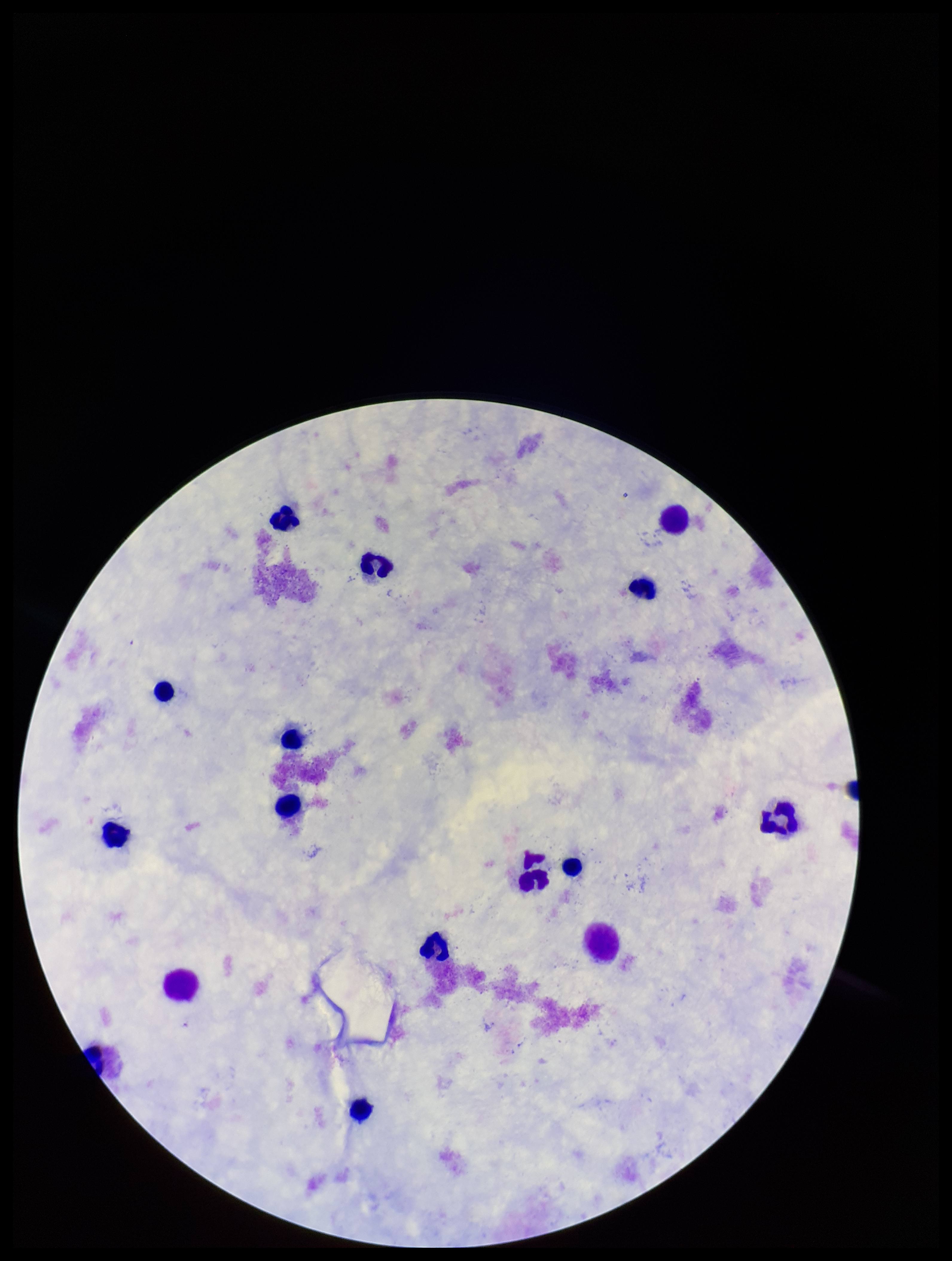

Summary:
  - Leukocyte count: 15
  - Patient malaria status: negative
  - Plasmodium parasites: none seen
  - Stain: Giemsa
  - Field of view: one from this slide
  - Image size: 952×1261 pixels
  - Capture: smartphone photograph through the microscope eyepiece
  - Preparation: thick
  - Parasite count: 0